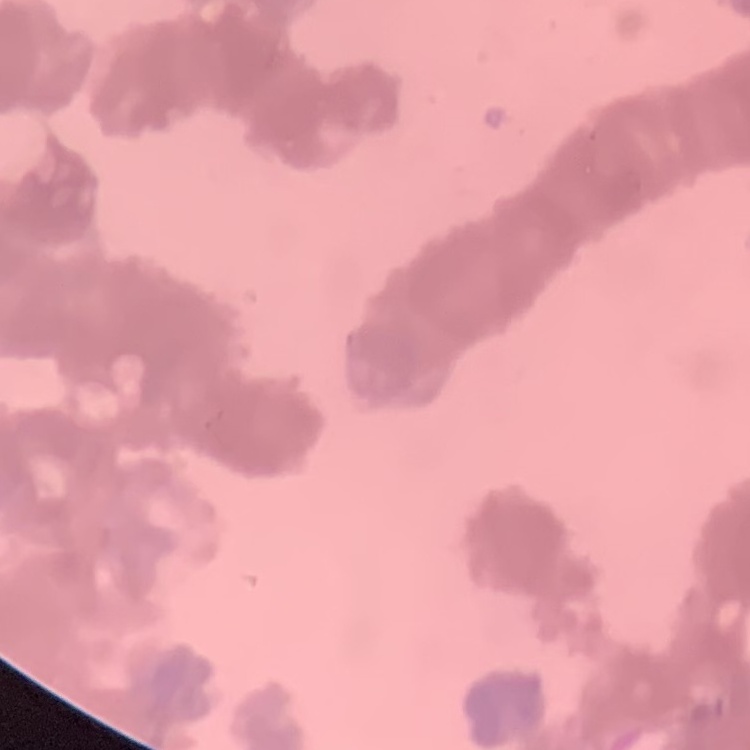
Summary:
  - Erythrocyte morphology: rouleaux formation
  - Preparation: thin blood film
  - Stain: Field's or Giemsa
  - Image type: one tile cut from a larger photomicrograph